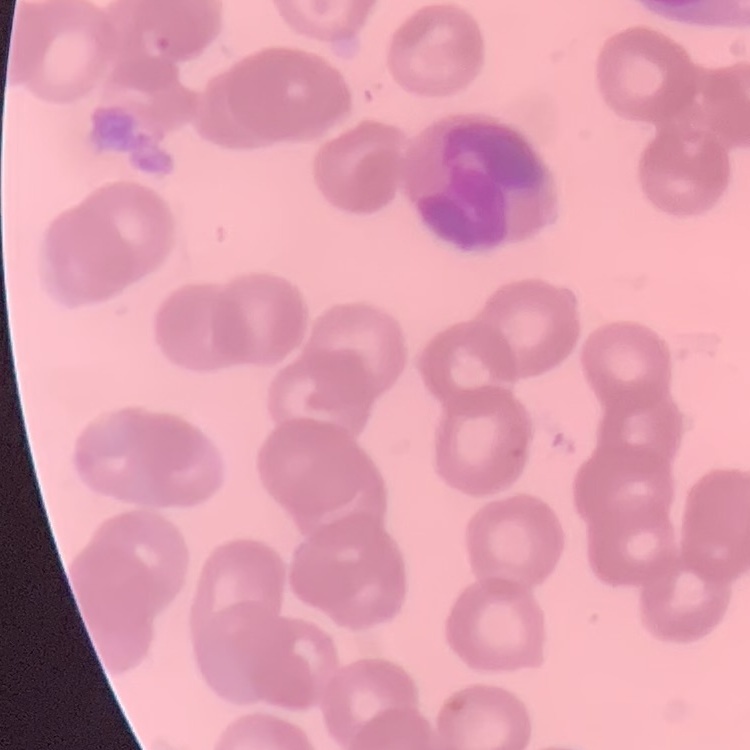
Summary:
  - Red blood cell morphology: rouleaux formation
  - Preparation: thin blood smear
  - Stain: Field's or Giemsa
  - Image type: one tile cut from a larger photomicrograph